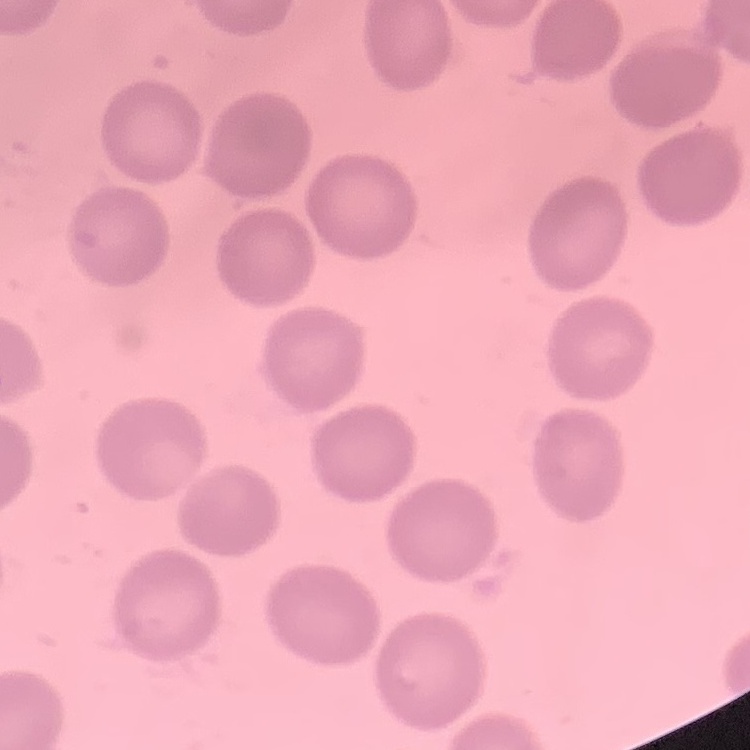

red blood cell morphology = no rouleaux formation
stain = Field's or Giemsa
image type = one tile cut from a larger photomicrograph
preparation = thin blood film